Report the malaria status of this cell.
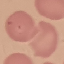
Uninfected.

stain = Giemsa
preparation = thin blood film
image type = automatically extracted cell patch, resized to 64 × 64 pixels
capture = smartphone camera at the microscope eyepiece